Give the preparation type.
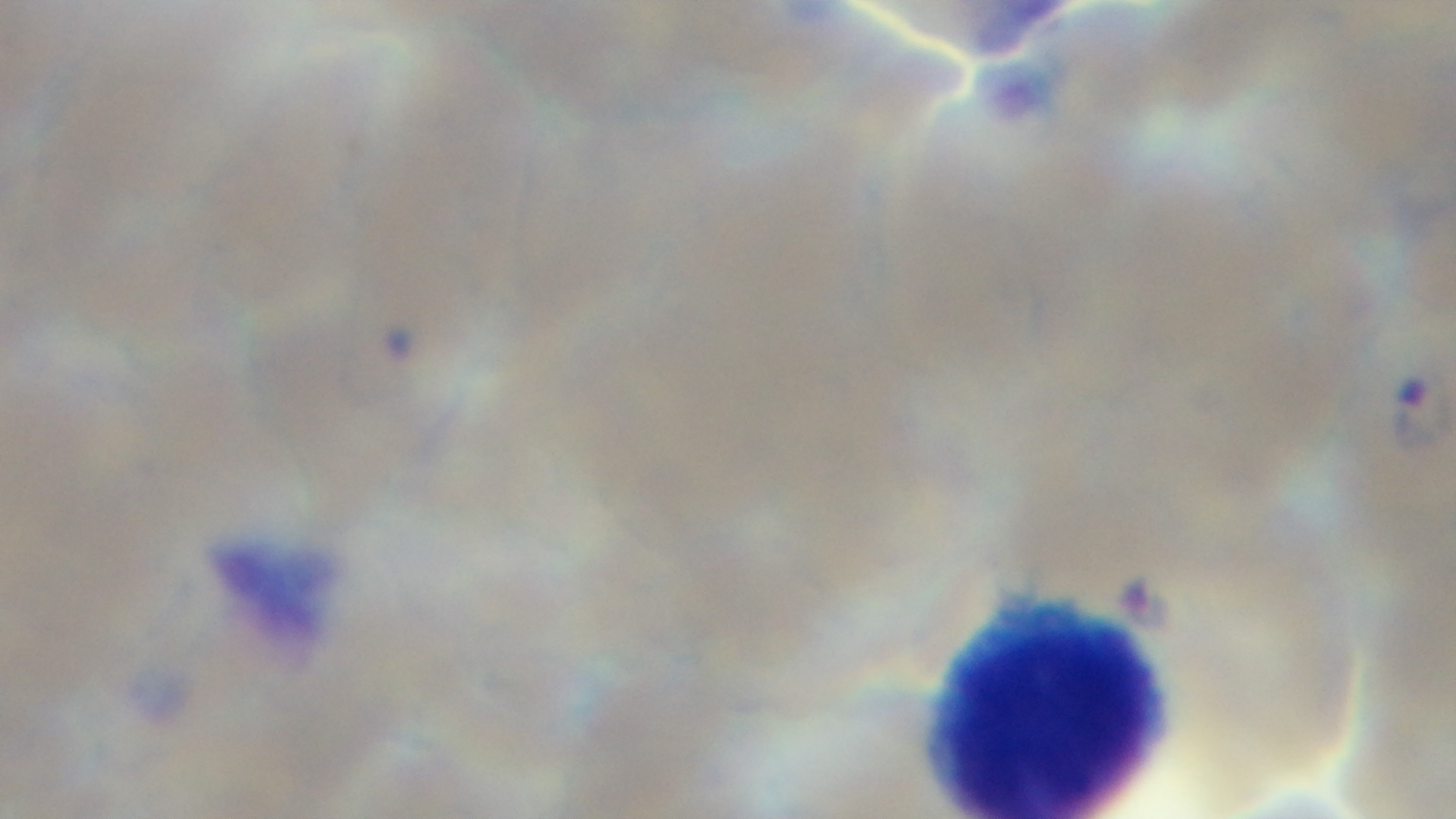

Thin.

Summary:
  - Modality: light microscopy
  - Field of view: single
  - Objective: 100x oil immersion
  - Stain: Giemsa
  - Malaria status: infected
  - Capture: mounted 4K digital camera